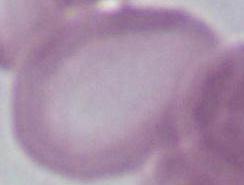

An erythrocyte is shown. Micrograph. 1000x magnification.